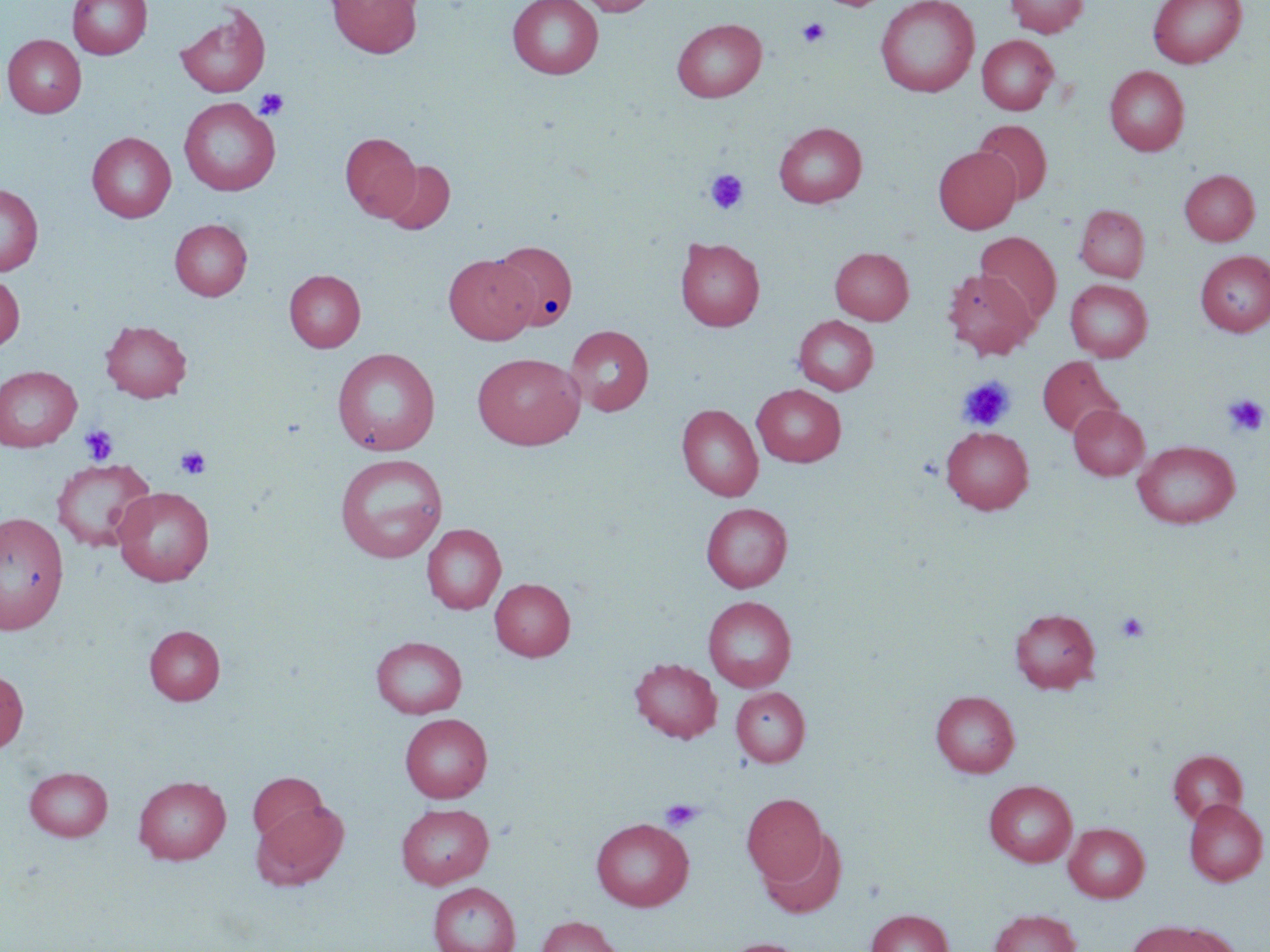
slide-level diagnosis = negative for blood parasites
uninfected red blood cell locations = approximate bounding boxes as [x1, y1, x2, y2] in pixels: [68, 0, 152, 59], [327, 0, 422, 58], [507, 0, 603, 80], [577, 0, 659, 16], [818, 0, 890, 10], [875, 0, 980, 97], [1005, 0, 1088, 37], [1148, 0, 1246, 67], [175, 4, 271, 98], [672, 18, 767, 102], [977, 34, 1059, 115], [3, 35, 86, 117], [1104, 66, 1189, 156], [179, 97, 281, 196], [973, 119, 1052, 204], [774, 122, 867, 208], [87, 132, 176, 222], [341, 132, 420, 221], [933, 146, 1021, 233], [381, 160, 455, 235], [1180, 170, 1259, 245], [0, 184, 43, 276], [1075, 204, 1150, 282], [169, 219, 252, 301], [976, 232, 1061, 325], [675, 237, 765, 332], [492, 240, 578, 331], [830, 247, 914, 324], [1196, 250, 1270, 336], [443, 254, 536, 344], [284, 269, 365, 352], [942, 269, 1038, 359], [0, 273, 24, 353], [1065, 279, 1152, 362], [793, 315, 879, 395], [101, 320, 192, 402], [565, 324, 653, 416], [332, 347, 440, 456], [472, 352, 585, 450], [1038, 356, 1123, 438], [0, 366, 81, 451], [752, 384, 846, 467], [677, 404, 763, 501], [1069, 404, 1149, 480], [941, 426, 1034, 514], [1133, 440, 1240, 529], [335, 453, 448, 562], [51, 458, 156, 552], [113, 487, 214, 586], [701, 503, 792, 592], [0, 511, 69, 634], [421, 523, 506, 614], [490, 578, 575, 660], [703, 596, 797, 692], [1010, 608, 1100, 692], [144, 624, 225, 705], [371, 636, 467, 718], [629, 657, 722, 743], [0, 668, 28, 753], [731, 686, 810, 767], [931, 691, 1019, 778], [400, 713, 492, 802], [1168, 750, 1248, 825], [24, 766, 112, 841], [247, 772, 331, 847], [133, 775, 230, 864], [984, 780, 1077, 867], [742, 793, 827, 884], [1185, 799, 1268, 885], [254, 800, 349, 889], [395, 803, 494, 888], [592, 818, 693, 911], [1064, 822, 1149, 902], [759, 829, 849, 920], [428, 882, 520, 952], [866, 909, 952, 952], [988, 909, 1081, 952], [535, 915, 625, 952], [1128, 921, 1233, 952], [719, 937, 811, 952]
modality = optical microscopy
magnification = 1000x
stain = May-Grünwald-Giemsa
platelet locations = approximate bounding boxes as [x1, y1, x2, y2] in pixels: [797, 18, 829, 47], [254, 88, 290, 121], [704, 169, 748, 215], [957, 376, 1016, 431], [1223, 395, 1268, 437], [79, 424, 119, 466], [175, 445, 211, 480], [1116, 611, 1150, 643], [660, 799, 704, 832]
image size = 1270×952 pixels
preparation = thin blood film
field of view = one of a larger specimen